Assess for malaria.
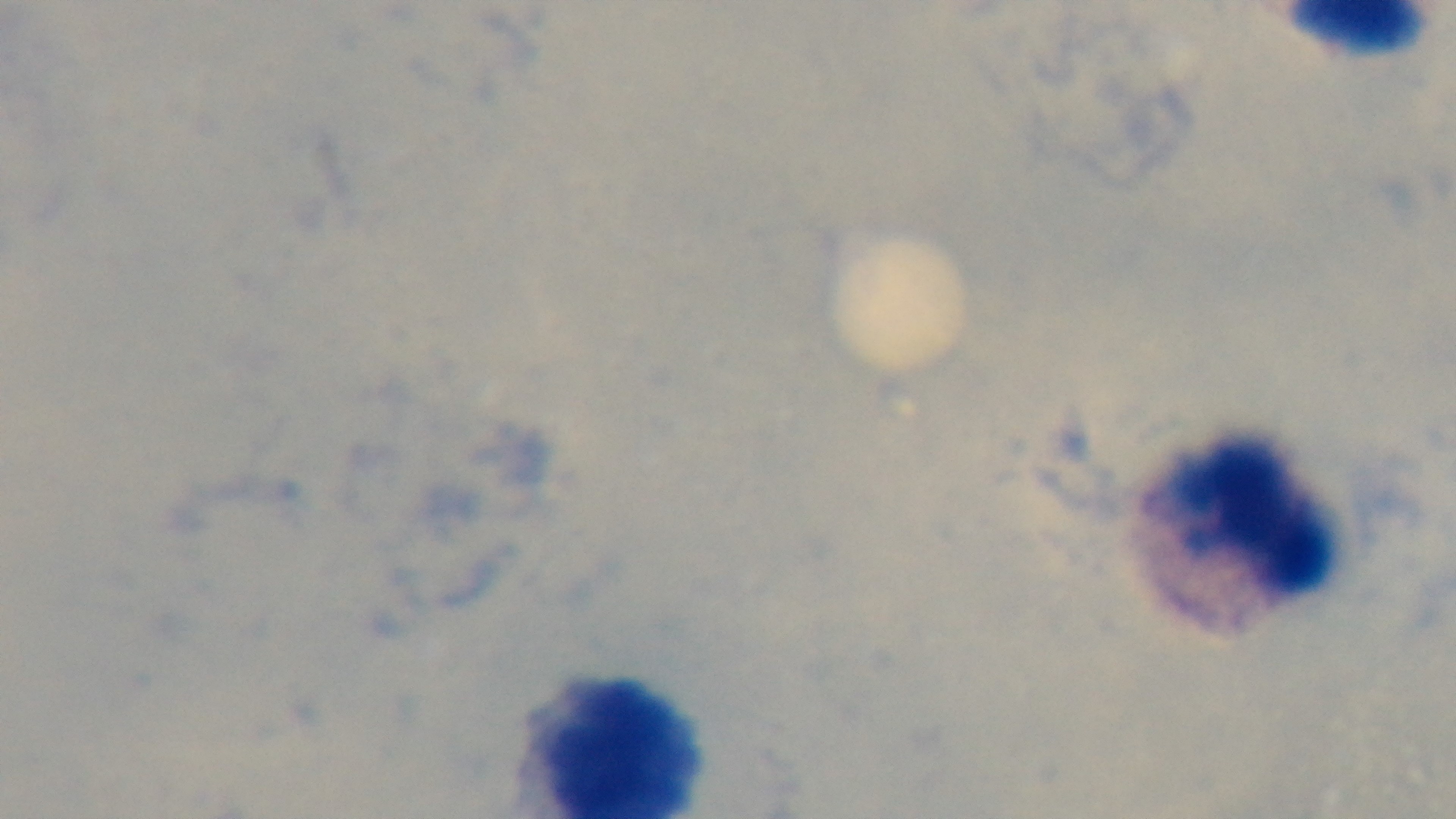
Negative.

Preparation: thick. Giemsa stain. Captured with a mounted 4K digital camera. One field from the slide. Photomicrograph. 100x oil-immersion objective.